Describe the morphology of the red blood cells.
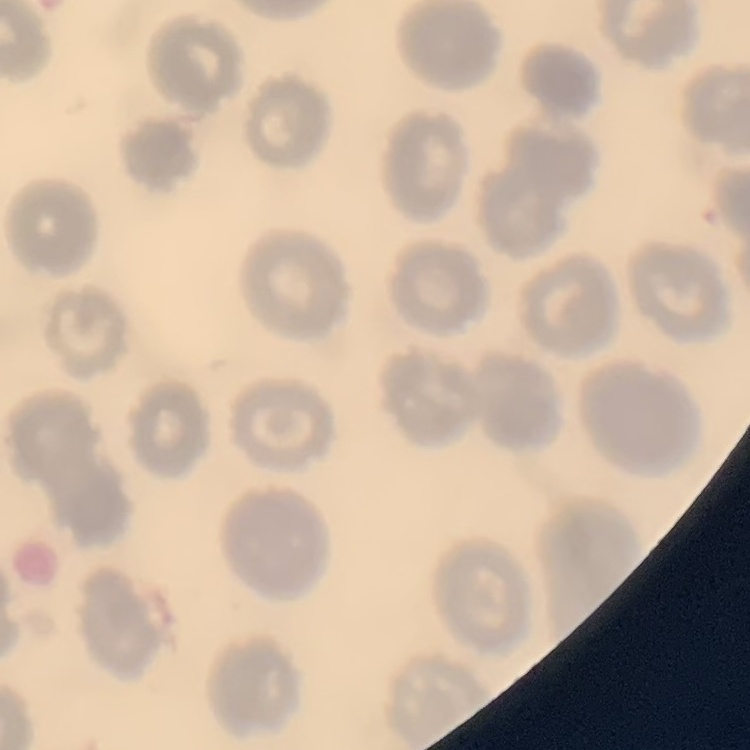

They show no rouleaux formation.

preparation = thin blood smear
image type = square crop of a larger photomicrograph
stain = Field's or Giemsa